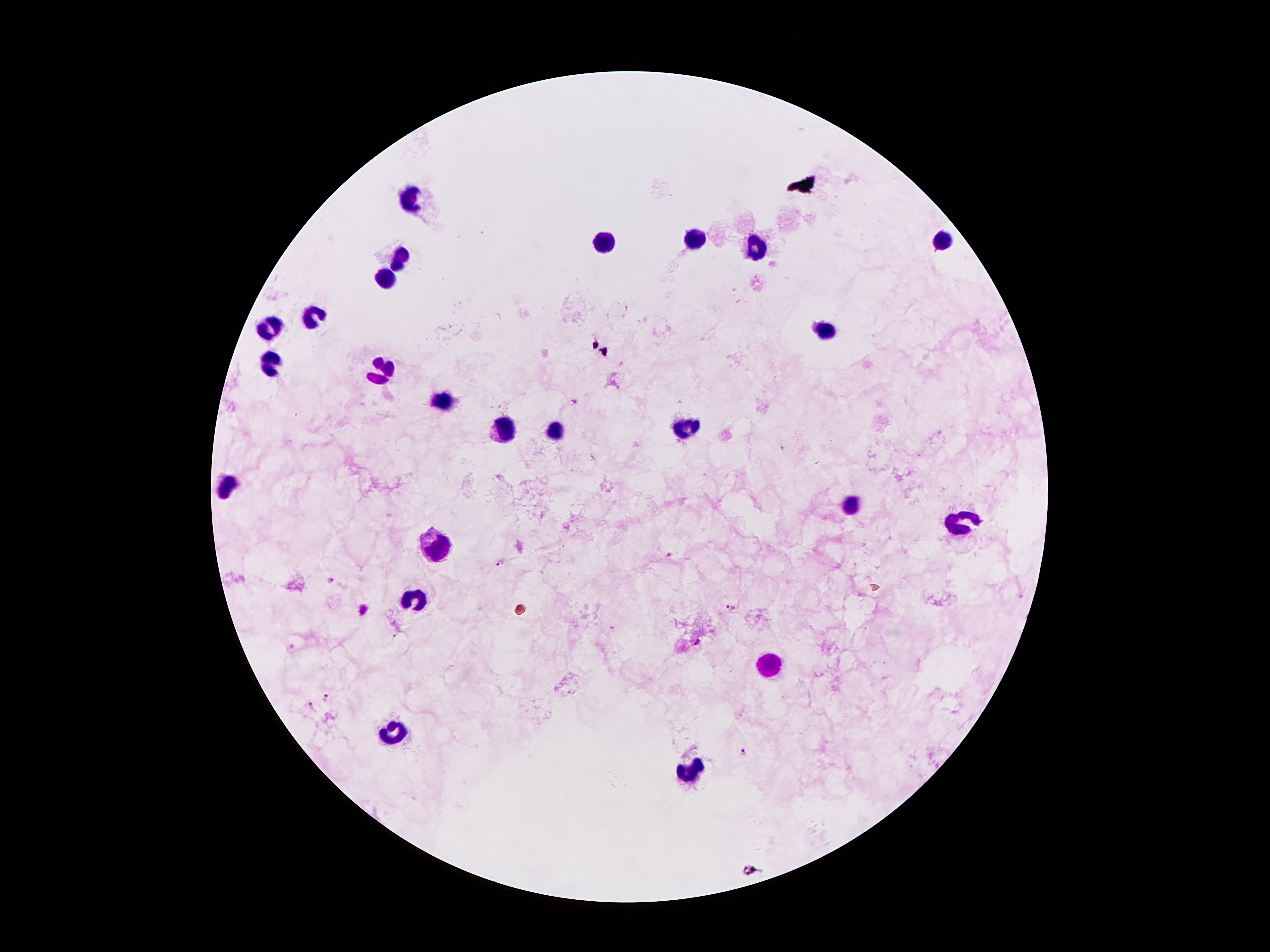
coordinate format = approximate object centers, in pixels from the top-left corner
leukocyte locations = (x=414, y=194), (x=603, y=239), (x=693, y=239), (x=941, y=239), (x=756, y=248), (x=402, y=255), (x=385, y=281), (x=315, y=318), (x=271, y=326), (x=826, y=329), (x=269, y=363), (x=385, y=372), (x=442, y=400), (x=686, y=427), (x=500, y=430), (x=556, y=430), (x=231, y=482), (x=850, y=504), (x=961, y=523), (x=435, y=544), (x=413, y=591), (x=770, y=666), (x=395, y=734), (x=689, y=774)
Plasmodium parasite locations = (x=574, y=401), (x=669, y=554), (x=501, y=562), (x=333, y=582), (x=731, y=608), (x=698, y=643), (x=327, y=699), (x=312, y=707), (x=744, y=752), (x=754, y=871)
capture = smartphone through the microscope eyepiece
image size = 1270×952 pixels
patient malaria status = infected with Plasmodium falciparum
magnification = 100x
field of view = single
stain = Giemsa
preparation = thick blood film